State the blood parasite species.
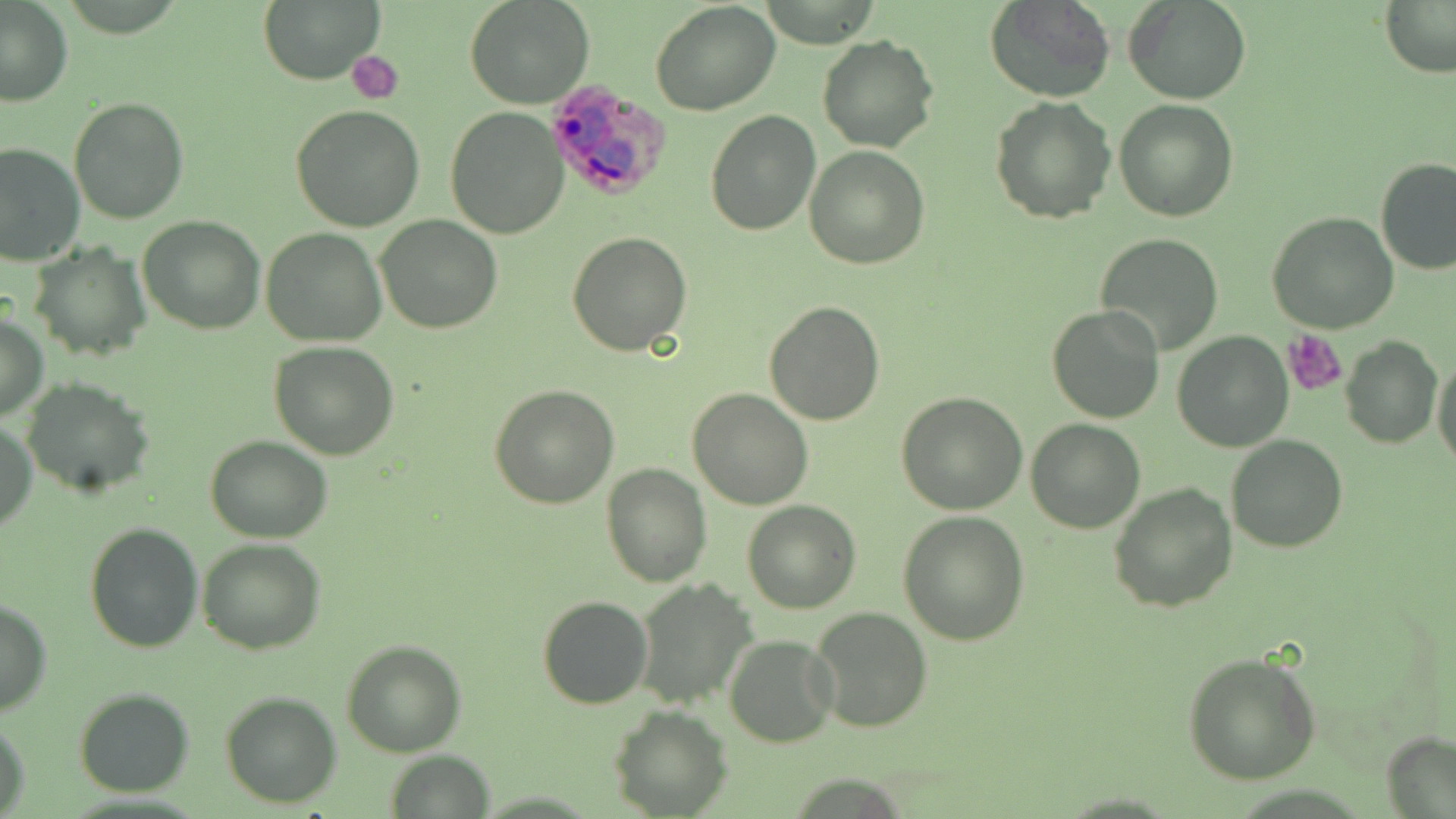

Plasmodium ovale.

uninfected red blood cell locations = approximate bounding boxes as [x1, y1, x2, y2] in pixels: [257, 0, 383, 87], [466, 0, 594, 109], [984, 0, 1116, 103], [1123, 0, 1252, 104], [1380, 0, 1456, 77], [1, 1, 75, 106], [649, 2, 781, 116], [817, 34, 940, 154], [989, 96, 1117, 225], [69, 97, 192, 224], [1114, 100, 1239, 222], [291, 104, 425, 231], [444, 108, 569, 240], [704, 110, 821, 237], [0, 143, 84, 265], [804, 144, 930, 268], [1374, 158, 1456, 275], [1268, 211, 1398, 334], [138, 215, 267, 334], [375, 216, 503, 334], [261, 228, 388, 347], [567, 232, 691, 355], [1094, 233, 1224, 355], [30, 242, 150, 362], [763, 300, 886, 425], [1047, 304, 1165, 424], [0, 308, 48, 422], [1171, 331, 1293, 452], [1341, 336, 1441, 450], [270, 341, 399, 459], [1432, 356, 1454, 469], [21, 378, 154, 496], [489, 384, 620, 508], [687, 388, 812, 511], [896, 390, 1026, 514], [1, 417, 37, 533], [1026, 418, 1146, 533], [1226, 433, 1347, 552], [205, 434, 331, 543], [603, 463, 712, 585], [1109, 483, 1237, 612], [742, 499, 861, 614], [898, 510, 1029, 645], [83, 521, 202, 652], [197, 539, 327, 655], [633, 578, 758, 710], [537, 595, 653, 709], [0, 598, 53, 716], [808, 605, 930, 734], [724, 635, 839, 747], [341, 640, 467, 757], [1182, 650, 1321, 784], [75, 688, 194, 798], [221, 691, 341, 807], [610, 706, 731, 817], [1, 714, 31, 818], [1382, 733, 1454, 816], [385, 750, 494, 819]
modality = optical microscopy
image size = 1456×819 pixels
magnification = 1000x
field of view = one of a larger specimen
platelet locations = approximate bounding boxes as [x1, y1, x2, y2] in pixels: [351, 51, 403, 102], [1282, 330, 1349, 396]
preparation = thin blood smear
stain = May-Grünwald-Giemsa
Plasmodium ovale-infected red blood cell locations = approximate bounding boxes as [x1, y1, x2, y2] in pixels: [544, 77, 673, 204]